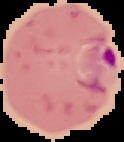
Image is 124×142 pixels. From a thin blood smear. Segmented cell region on a black background. Malaria status: parasitized.